Give the position of every malaria parasite.
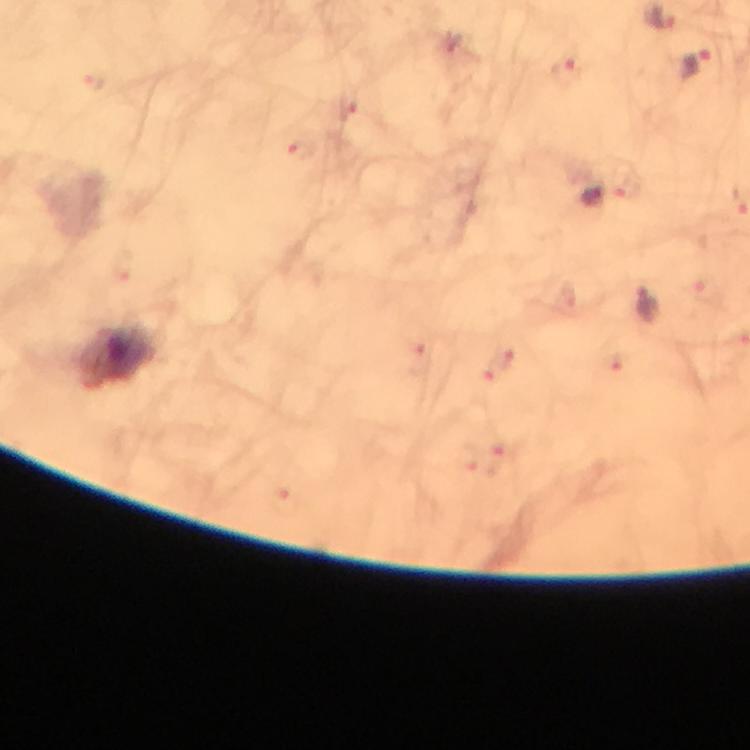

Approximate centers as (x, y) in pixels.
Malaria parasites: (696, 65), (605, 195), (648, 302).

Summary:
  - Stain: Giemsa
  - Immersion oil: used
  - Preparation: thick smear
  - Cropped from: a single field of view
  - Context: from a malaria diagnostic workup
  - Image size: 750×750 pixels
  - Capture: smartphone camera through the microscope
  - Magnification: 100x